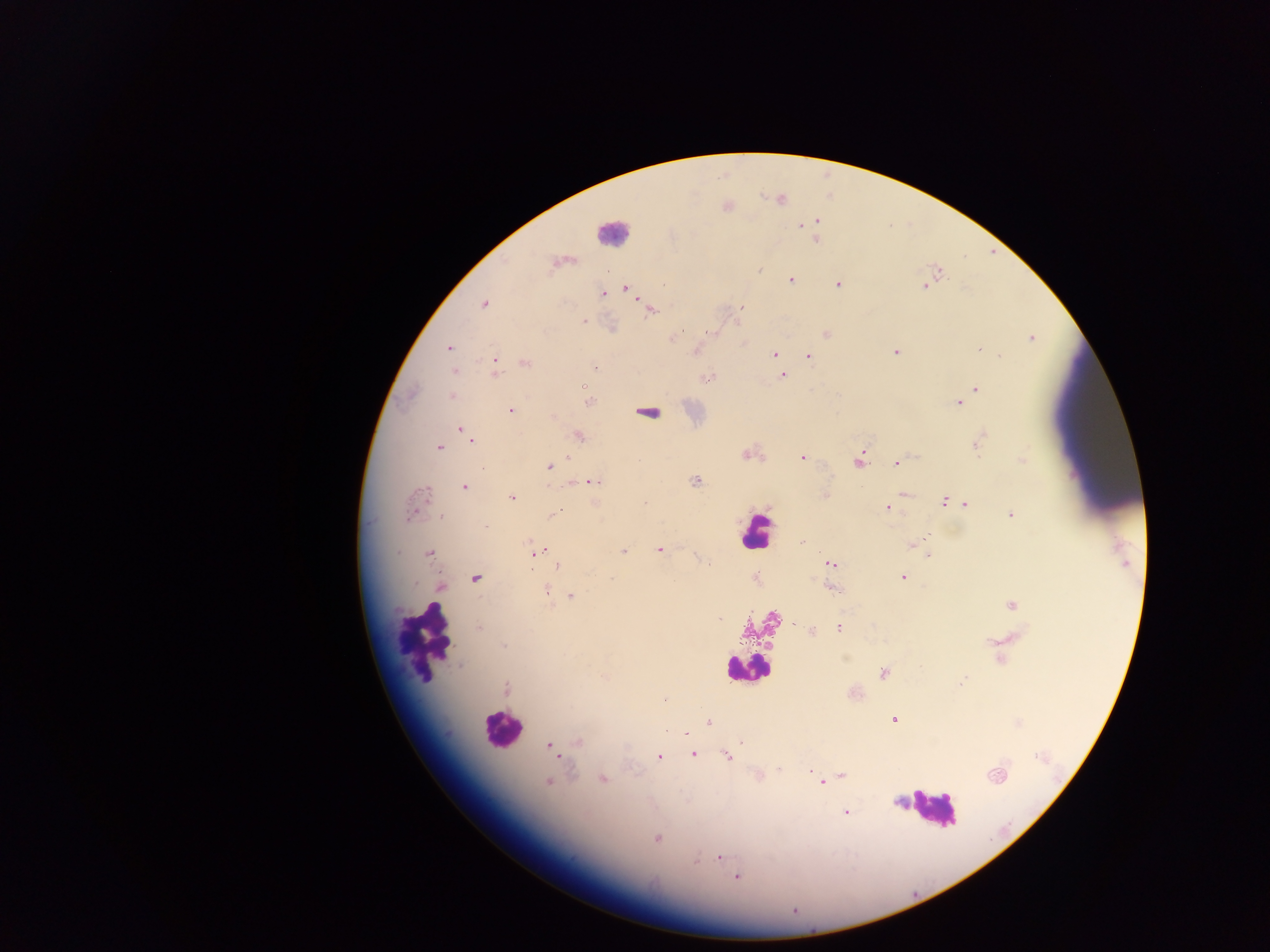

Approximate centers as x y in pixels.
Summary:
  - Malaria parasite locations: 779 199; 725 206; 816 221; 800 225; 804 226; 815 239; 559 262; 758 269; 790 279; 837 283; 924 286; 624 288; 602 293; 484 303; 740 306; 650 309; 582 320; 611 327; 826 334; 673 338; 1031 338; 448 347; 979 349; 695 351; 895 351; 774 354; 808 356; 495 362; 524 362; 595 366; 454 370; 493 372; 782 375; 707 376; 583 385; 976 389; 451 396; 588 402; 958 403; 509 409; 647 412; 552 416; 462 429; 578 435; 471 438; 978 443; 440 447; 747 454; 801 457; 859 460; 1022 460; 897 462; 548 466; 590 481; 694 481; 463 486; 903 494; 824 495; 512 497; 944 501; 962 501; 645 502; 965 503; 417 504; 886 507; 1011 513; 555 514; 443 517; 487 527; 928 535; 802 541; 912 545; 658 549; 539 550; 622 551; 429 552; 927 555; 830 564; 709 565; 558 566; 902 577; 474 578; 756 578; 440 586; 829 587; 547 590; 571 596; 1012 604; 718 618; 840 627; 479 628; 811 630; 503 646; 884 672; 961 682; 506 690; 853 692; 664 700; 893 719; 709 723; 741 740; 577 743; 549 746; 555 754; 693 754; 727 755; 658 756; 779 769; 842 775; 995 775; 758 776; 603 779; 549 781; 821 783; 846 813; 656 838; 719 857; 737 876; 794 910
  - Leukocyte locations: 613 233; 756 531; 761 625; 424 641; 747 667; 501 729; 935 809
  - Country: Ghana
  - Preparation: thick blood smear
  - Capture: mobile-phone photograph through a microscope
  - Image size: 1270×952 pixels
  - Field of view: single